Locate every blood parasite and identify its species.
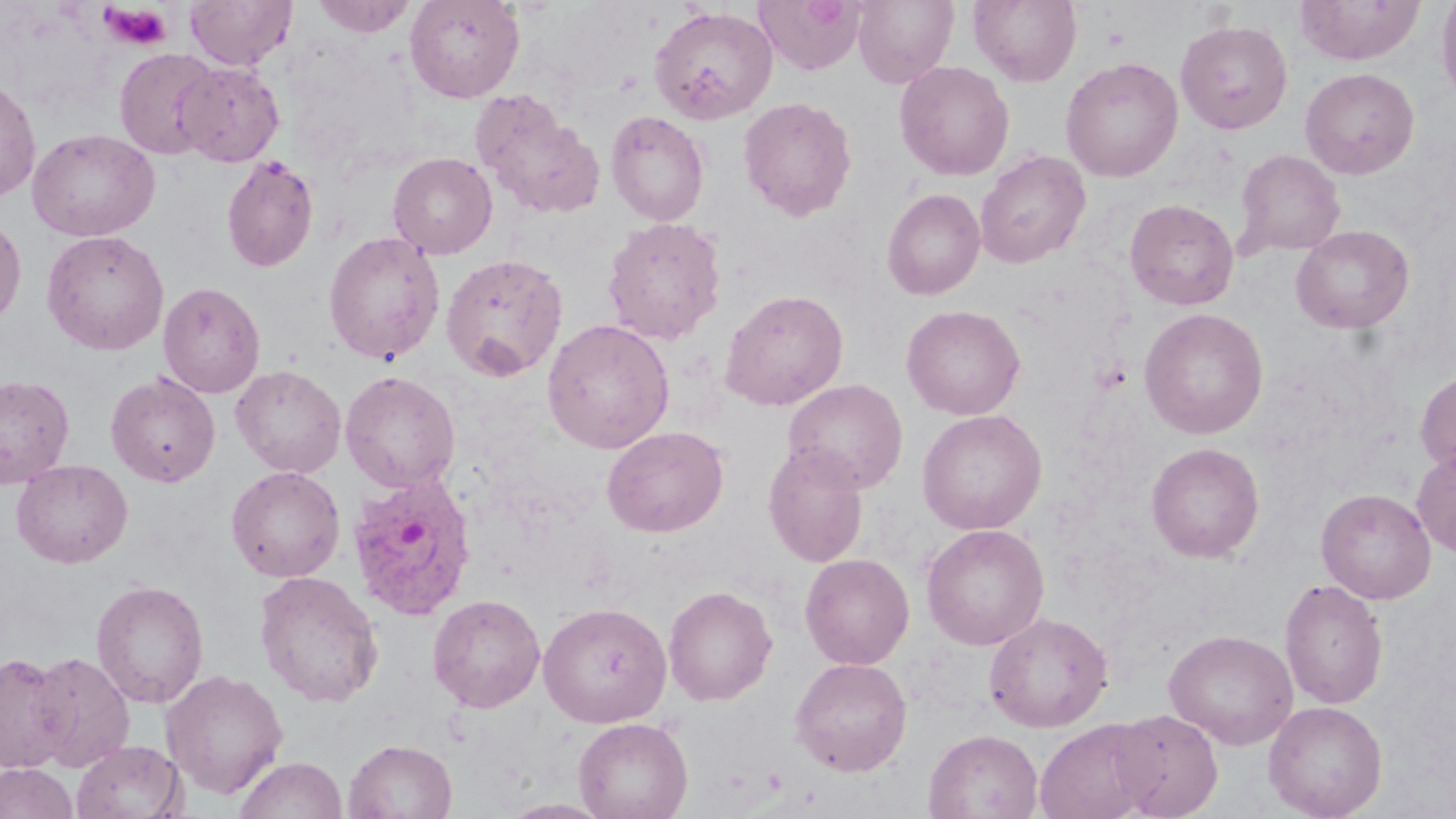

Approximate bounding boxes as (x1, y1, x2, y2) in pixels.
Plasmodium ovale-infected red blood cells: (347, 472, 478, 621).
No Plasmodium falciparum, Plasmodium malariae, Plasmodium vivax, Babesia divergens, or Trypanosoma brucei observed.

Summary:
  - Platelet locations: (98, 4, 173, 51)
  - Uninfected red blood cell locations: (185, 0, 297, 70), (310, 0, 418, 36), (404, 0, 525, 103), (851, 0, 959, 87), (969, 0, 1082, 86), (1436, 0, 1456, 108), (754, 1, 866, 75), (1296, 1, 1426, 65), (648, 6, 778, 125), (1175, 19, 1293, 134), (113, 48, 222, 160), (1060, 57, 1183, 181), (174, 61, 285, 166), (894, 61, 1015, 180), (1300, 67, 1420, 179), (0, 77, 41, 203), (470, 89, 604, 220), (738, 97, 857, 221), (606, 110, 710, 226), (27, 128, 159, 242), (1232, 149, 1345, 259), (975, 150, 1091, 268), (388, 152, 498, 259), (221, 155, 319, 273), (882, 188, 985, 300), (1124, 198, 1239, 310), (0, 215, 26, 326), (602, 216, 727, 345), (1292, 224, 1415, 333), (42, 229, 169, 355), (323, 231, 446, 365), (441, 252, 569, 382), (158, 281, 266, 398), (719, 289, 849, 411), (901, 304, 1025, 420), (1139, 307, 1269, 439), (542, 318, 675, 454), (230, 365, 347, 477), (1416, 369, 1456, 478), (340, 370, 460, 493), (106, 371, 220, 488), (0, 374, 75, 488), (782, 379, 908, 494), (916, 409, 1047, 535), (603, 426, 729, 537), (1146, 442, 1265, 562), (763, 443, 869, 568), (1412, 444, 1456, 558), (11, 459, 133, 568), (226, 465, 345, 582), (1316, 488, 1436, 604), (920, 523, 1050, 650), (800, 553, 915, 669), (254, 571, 384, 707), (1279, 577, 1389, 709), (91, 579, 209, 708), (663, 585, 777, 706), (427, 594, 546, 713), (538, 602, 672, 727), (983, 611, 1114, 732), (1164, 628, 1299, 749), (0, 651, 72, 773), (28, 651, 134, 772), (790, 657, 912, 776), (161, 669, 288, 799), (1263, 700, 1387, 818), (1110, 708, 1223, 818), (573, 717, 692, 819), (1034, 719, 1158, 819), (924, 728, 1043, 819), (343, 738, 457, 819), (71, 740, 187, 819), (234, 756, 346, 819), (0, 763, 77, 819), (497, 798, 614, 818)
  - Slide-level diagnosis: Plasmodium ovale
  - Magnification: 1000x
  - Modality: optical microscopy
  - Field of view: single
  - Image size: 1456×819 pixels
  - Stain: May-Grünwald-Giemsa
  - Preparation: thin blood smear